Classify this cell by malaria status.
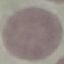
It is uninfected.

Thin blood film. Giemsa stain. Automatically extracted cell patch, resized to 64 × 64 pixels. Acquired by smartphone through the microscope eyepiece.